Name the parasite shown.
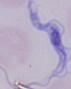

A trypanosome.

Summary:
  - Magnification: 1000x
  - Modality: photomicrograph